Assess the morphology of the erythrocytes.
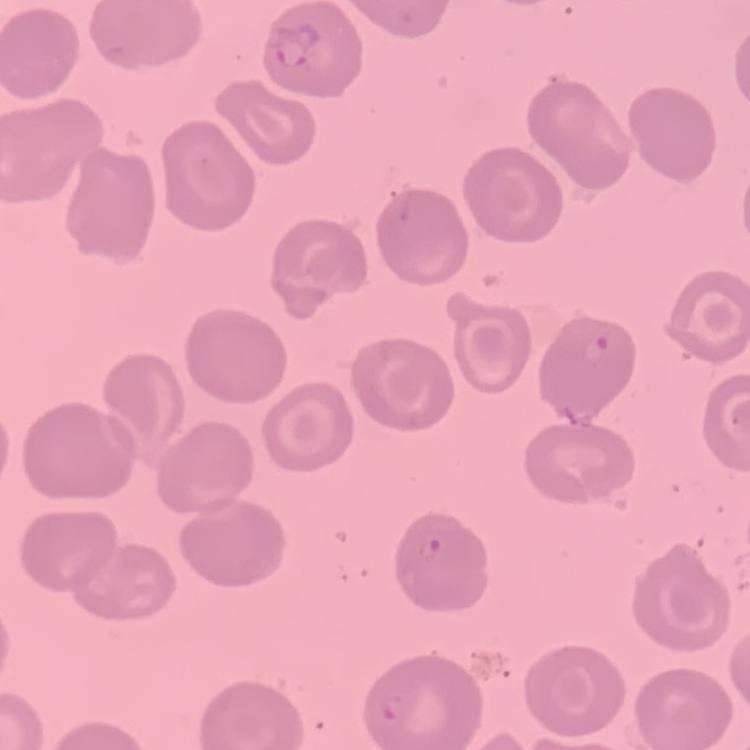
They show no rouleaux formation.

Summary:
  - Preparation: thin blood film
  - Stain: Field's or Giemsa
  - Image type: one tile cut from a larger photomicrograph